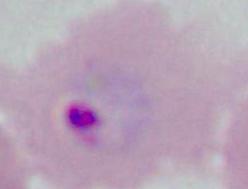 A Plasmodium parasite is seen. Captured at either 400x or 1000x magnification. Micrograph.